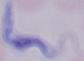

Micrograph. 1000x magnification. A trypanosome is seen.